State the blood parasite species.
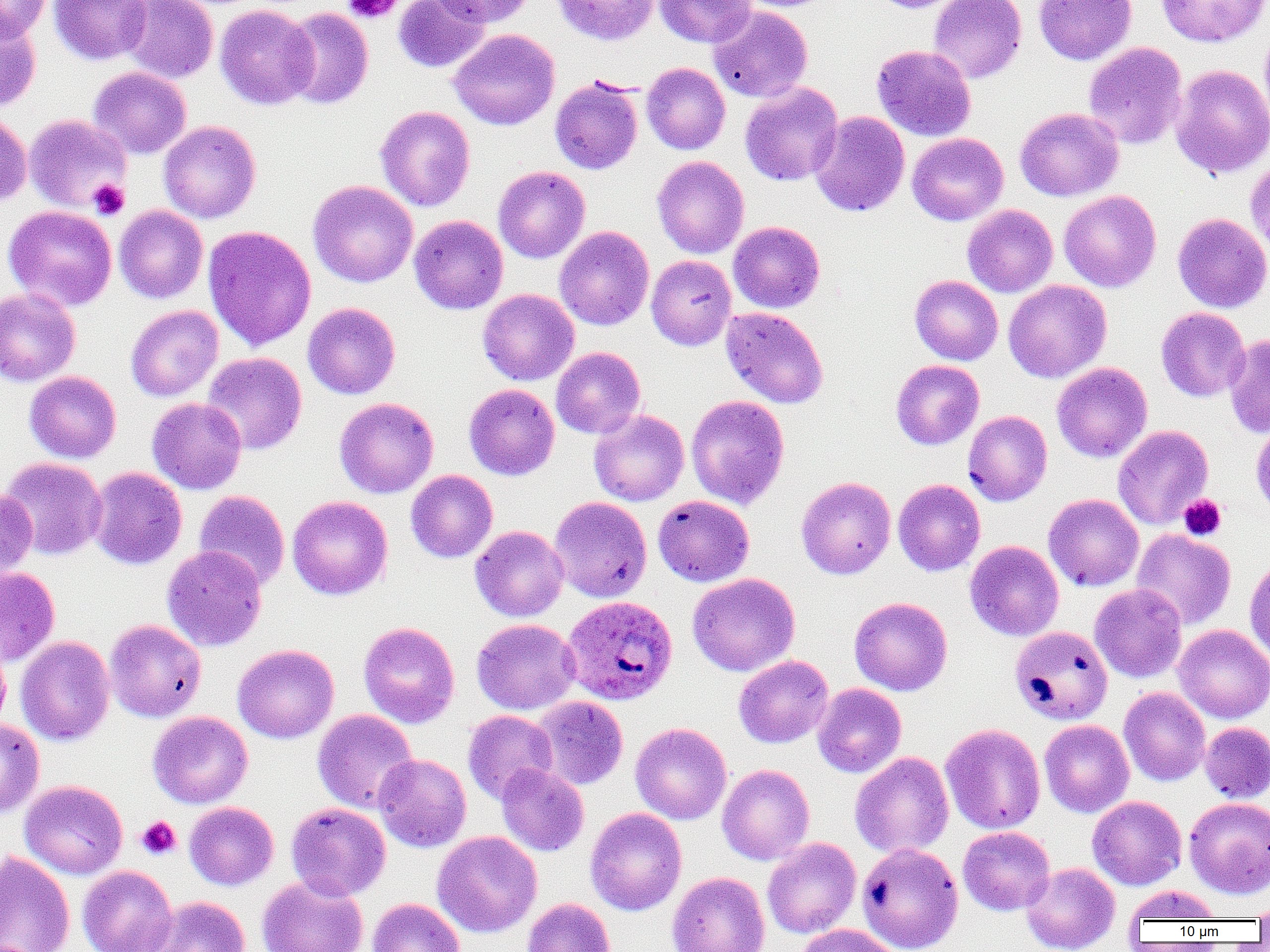
Plasmodium ovale.

Approximate bounding boxes as (x1, y1, x2, y2) in pixels. Plasmodium ovale-infected red blood cell locations: (561, 595, 678, 704). Platelet locations: (343, 0, 402, 23), (89, 179, 129, 219), (1178, 494, 1226, 541), (136, 816, 181, 860). Uninfected red blood cell locations: (0, 0, 51, 41), (50, 0, 152, 65), (120, 0, 219, 83), (388, 0, 482, 141), (393, 0, 489, 72), (428, 0, 535, 27), (551, 0, 659, 46), (655, 0, 755, 48), (732, 0, 840, 12), (869, 0, 965, 13), (928, 0, 1027, 84), (1033, 0, 1136, 65), (1156, 0, 1269, 47), (215, 4, 318, 109), (708, 5, 813, 102), (282, 7, 373, 109), (0, 12, 41, 111), (1259, 24, 1270, 129), (449, 29, 560, 130), (1083, 42, 1187, 150), (872, 45, 976, 141), (642, 62, 730, 154), (1170, 64, 1270, 179), (88, 67, 191, 159), (550, 76, 643, 175), (740, 82, 843, 186), (375, 106, 475, 211), (1015, 107, 1124, 201), (0, 111, 32, 206), (810, 111, 909, 217), (24, 114, 132, 213), (158, 120, 261, 223), (907, 133, 1008, 226), (1245, 153, 1270, 257), (652, 156, 749, 259), (493, 166, 590, 264), (307, 180, 418, 288), (1059, 190, 1161, 292), (962, 204, 1058, 297), (4, 205, 117, 311), (114, 205, 208, 304), (1173, 213, 1270, 313), (409, 215, 508, 315), (728, 221, 825, 313), (203, 225, 316, 351), (554, 226, 654, 330), (647, 255, 736, 350), (910, 275, 1003, 365), (1003, 280, 1111, 383), (0, 287, 80, 386), (477, 289, 579, 385), (302, 302, 401, 399), (125, 305, 223, 402), (721, 307, 829, 409), (1156, 307, 1250, 401), (1224, 332, 1270, 439), (551, 347, 645, 438), (202, 352, 307, 455), (891, 359, 984, 450), (1052, 362, 1152, 463), (24, 371, 121, 463), (464, 384, 560, 481), (686, 395, 790, 510), (147, 397, 247, 494), (335, 397, 438, 499), (588, 409, 689, 506), (963, 410, 1052, 506), (1113, 425, 1213, 530), (0, 457, 107, 560), (87, 467, 187, 570), (406, 470, 498, 563), (796, 476, 896, 579), (893, 478, 985, 576), (0, 489, 38, 580), (194, 490, 290, 589), (1043, 493, 1144, 591), (287, 495, 393, 600), (653, 495, 754, 586), (549, 496, 652, 602), (470, 525, 569, 622), (1132, 529, 1236, 630), (965, 540, 1064, 641), (161, 545, 267, 652), (1244, 555, 1270, 663), (0, 566, 60, 665), (687, 572, 800, 676), (1089, 584, 1187, 682), (849, 596, 952, 696), (471, 618, 580, 715), (105, 619, 206, 722), (359, 622, 459, 728), (1174, 624, 1270, 723), (1010, 625, 1113, 725), (0, 636, 11, 737), (15, 636, 115, 745), (232, 644, 339, 744), (734, 655, 834, 747), (813, 683, 906, 778), (1119, 687, 1211, 786), (531, 696, 628, 790), (312, 709, 418, 813), (463, 710, 557, 804), (148, 711, 252, 808), (0, 719, 44, 819), (1039, 719, 1134, 817), (1200, 722, 1270, 803), (630, 723, 731, 824), (941, 723, 1045, 834), (850, 751, 954, 858), (374, 754, 471, 852), (496, 763, 589, 856), (717, 764, 814, 865), (20, 780, 128, 879), (1087, 796, 1186, 890), (1184, 797, 1270, 898), (184, 801, 279, 890), (285, 802, 391, 901), (585, 808, 687, 916), (958, 826, 1055, 915), (432, 831, 542, 937), (762, 837, 861, 938), (857, 842, 964, 952), (0, 851, 75, 952), (1021, 862, 1120, 952), (77, 865, 177, 952), (667, 872, 770, 952), (257, 876, 368, 952), (1123, 885, 1224, 924), (148, 896, 250, 952), (1249, 896, 1270, 923), (367, 897, 465, 952), (522, 897, 615, 952), (795, 923, 899, 952). Thin blood film. Captured at 1000x magnification. Single field of view. Image is 1270×952 pixels. Optical microscopy.